Give the extent of all Plasmodium falciparum-infected red blood cells.
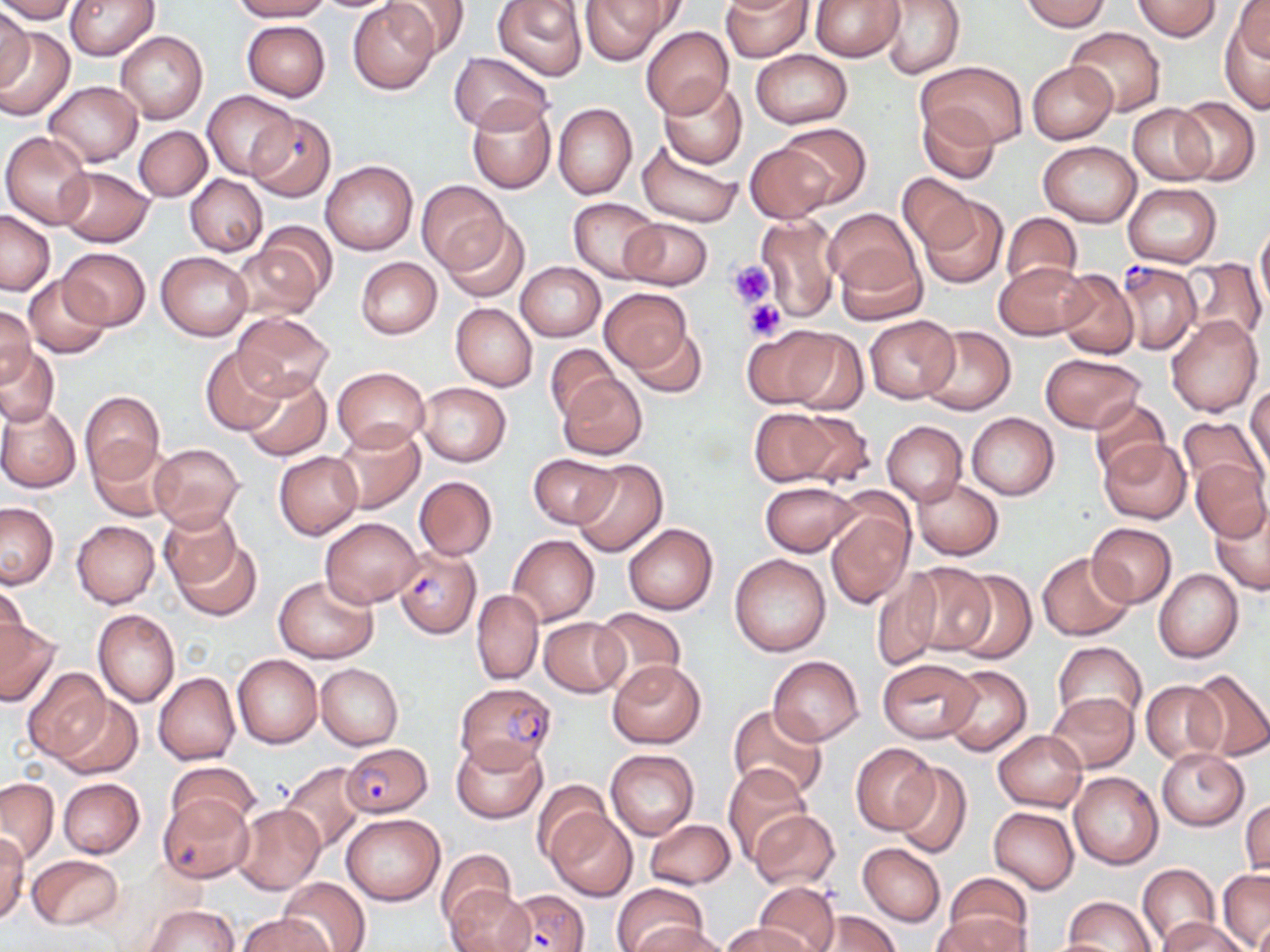

Approximate bounding boxes as (x1,y1)-(x2,y2) corner pairs in pixels.
Plasmodium falciparum-infected red blood cells: (246,113)-(336,202), (1115,260)-(1200,355), (393,545)-(480,639), (454,681)-(557,771), (341,740)-(433,818), (495,888)-(590,950).

slide_level_diagnosis: Plasmodium falciparum
preparation: thin blood smear
uninfected_red_blood_cell_locations: 'approximate bounding boxes as (x1,y1)-(x2,y2) corner pairs in pixels: (0,0)-(78,23), (66,0)-(160,60), (230,0)-(331,22), (349,0)-(440,95), (382,0)-(470,61), (579,0)-(675,64), (720,0)-(811,60), (880,0)-(965,79), (1021,0)-(1111,32), (493,1)-(587,81), (811,1)-(903,60), (1132,1)-(1222,40), (1231,2)-(1270,61), (0,7)-(32,89), (389,7)-(495,96), (1219,15)-(1270,112), (241,20)-(331,101), (1064,25)-(1166,117), (0,26)-(75,121), (640,26)-(733,119), (116,30)-(208,124), (6,39)-(115,149), (749,49)-(853,129), (449,51)-(554,135), (922,60)-(1028,149), (1027,61)-(1117,143), (658,80)-(747,168), (44,81)-(142,167), (202,89)-(298,180), (1175,96)-(1261,185), (466,98)-(556,194), (918,102)-(1000,183), (553,103)-(637,200), (1128,104)-(1215,185), (776,122)-(871,207), (134,125)-(211,201), (2,131)-(95,228), (637,140)-(741,228), (1038,141)-(1141,227), (744,143)-(836,223), (320,159)-(418,256), (56,166)-(154,247), (185,175)-(266,255), (897,175)-(981,253), (417,181)-(507,272), (1124,184)-(1222,268), (916,195)-(1010,290), (568,197)-(664,282), (0,209)-(54,294), (824,209)-(922,300), (1001,213)-(1085,292), (756,216)-(840,322), (442,217)-(531,302), (622,218)-(710,290), (1256,218)-(1270,316), (229,240)-(326,322), (833,245)-(928,326), (59,247)-(149,330), (156,251)-(252,341), (356,257)-(442,339), (1183,258)-(1266,345), (995,261)-(1091,341), (514,262)-(605,342), (1055,268)-(1140,360), (23,274)-(110,358), (601,288)-(693,373), (451,303)-(537,390), (0,307)-(37,389), (232,312)-(335,403), (864,315)-(959,404), (1165,316)-(1262,418), (621,320)-(709,397), (920,325)-(1015,415), (741,328)-(841,410), (545,343)-(619,421), (0,345)-(58,426), (200,347)-(286,435), (1040,353)-(1146,433), (330,367)-(430,452), (241,372)-(330,461), (556,374)-(647,460), (416,382)-(511,467), (1247,383)-(1269,476), (79,391)-(166,483), (1087,398)-(1172,481), (0,404)-(81,492), (747,407)-(845,487), (966,412)-(1059,500), (1179,416)-(1267,497), (330,420)-(426,514), (882,421)-(966,504), (1098,438)-(1192,525), (88,440)-(178,522), (148,442)-(245,533), (274,452)-(362,539), (529,454)-(617,528), (1190,457)-(1270,541), (571,458)-(668,558), (414,476)-(498,560), (912,478)-(1003,559), (761,481)-(859,556), (825,496)-(915,608), (0,501)-(58,589), (1209,501)-(1270,596), (157,508)-(242,592), (319,516)-(421,607), (72,520)-(159,608), (624,522)-(718,614), (1088,523)-(1175,607), (169,534)-(262,620), (508,534)-(598,625), (1037,552)-(1136,641), (730,554)-(831,657), (903,562)-(997,655), (1153,568)-(1244,663), (948,569)-(1037,665), (870,570)-(943,672), (273,574)-(378,663), (1,581)-(29,665), (472,589)-(543,685), (591,608)-(686,693), (93,609)-(179,706), (0,617)-(60,708), (540,617)-(628,696), (1053,641)-(1146,726), (232,653)-(322,749), (767,655)-(865,745), (878,658)-(981,742), (607,660)-(707,748), (315,662)-(403,749), (941,664)-(1032,755), (22,668)-(112,764), (1190,669)-(1269,761), (154,672)-(239,764), (1141,681)-(1225,764), (1046,691)-(1139,772), (51,695)-(143,779), (726,704)-(831,804), (993,730)-(1087,810), (451,735)-(548,823), (850,743)-(939,833), (1155,747)-(1250,831), (605,748)-(698,839), (166,759)-(259,832), (279,761)-(367,855), (891,763)-(972,858), (724,764)-(813,861), (1069,772)-(1163,870), (57,777)-(144,858), (0,778)-(58,864), (533,781)-(610,862), (158,795)-(254,883), (1240,797)-(1269,877), (232,803)-(325,895), (547,807)-(636,901), (989,807)-(1080,894), (748,810)-(840,890), (343,813)-(444,905), (644,819)-(735,888), (0,834)-(29,923), (858,843)-(946,925), (437,849)-(516,926), (27,854)-(124,930), (1137,865)-(1217,944), (1218,868)-(1269,950), (942,872)-(1033,947), (278,876)-(370,952), (445,883)-(533,952), (613,883)-(707,952), (755,883)-(839,951), (1061,897)-(1155,952), (142,904)-(239,952), (934,910)-(1028,952), (810,911)-(899,952), (1254,911)-(1270,952), (238,913)-(329,952), (1158,916)-(1250,951), (723,922)-(813,952), (637,925)-(733,952), (1032,937)-(1132,952)'
image_size: 1270×952 pixels
modality: optical microscopy
magnification: 1000x
platelet_locations: 'approximate bounding boxes as (x1,y1)-(x2,y2) corner pairs in pixels: (728,260)-(772,307), (744,299)-(786,341)'
field_of_view: single
stain: May-Grünwald-Giemsa